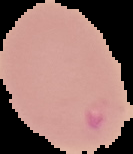

preparation: thin blood smear
image_size: 133×154 pixels
malaria_status: uninfected
image_type: segmented cell region with the area outside set to black